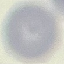
Summary:
  - Result: no malaria parasites seen
  - Image type: cell patch, automatically extracted from a larger field of view and resized to 64 × 64 pixels
  - Preparation: thin smear
  - Stain: Giemsa
  - Capture: smartphone camera at the microscope eyepiece